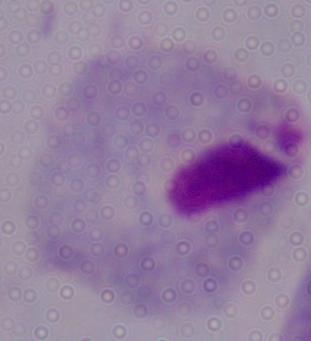
Summary:
  - Magnification: 1000x
  - Identification: trichomonad
  - Modality: micrograph